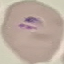

result = malaria parasites identified
image type = automatically extracted cell patch, resized to 64 × 64 pixels
capture = smartphone through the microscope eyepiece
stain = Giemsa
preparation = thin smear